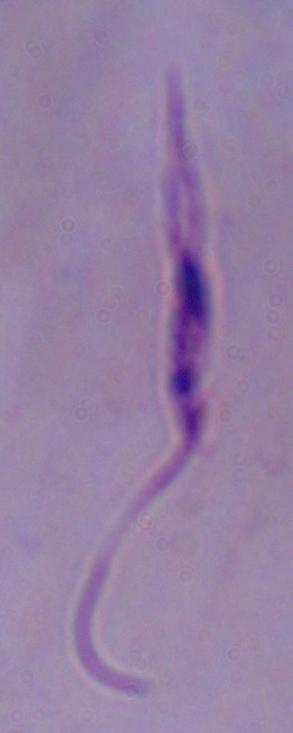
Summary:
  - Magnification: 1000x
  - Modality: photomicrograph
  - Identification: Leishmania